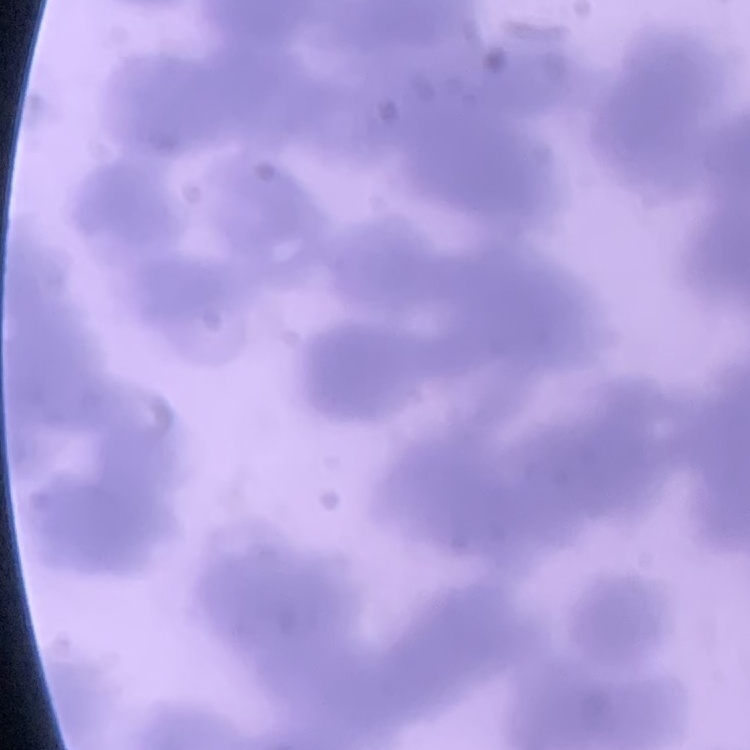
The erythrocytes exhibit rouleaux formation. Thin blood smear. Stained with either Field's or Giemsa. One tile cut from a larger photomicrograph.